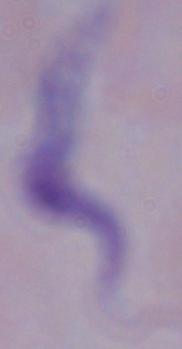 A trypanosome is shown. 1000x magnification. Photomicrograph.